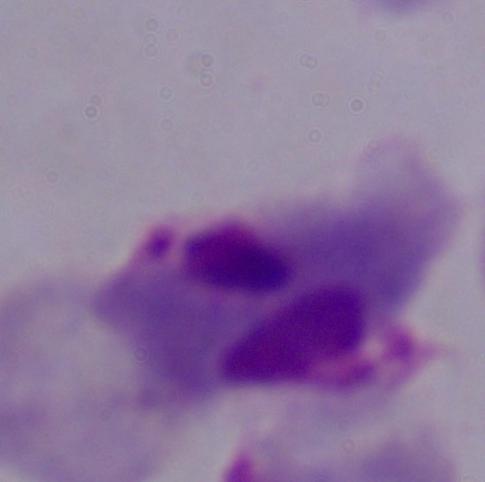

Summary:
  - Magnification: 1000x
  - Identification: trichomonad
  - Modality: photomicrograph